Report the malaria status of this cell.
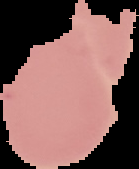

Uninfected.

Summary:
  - Image type: segmented cell region with the area outside set to black
  - Preparation: thin blood smear
  - Image size: 139×169 pixels